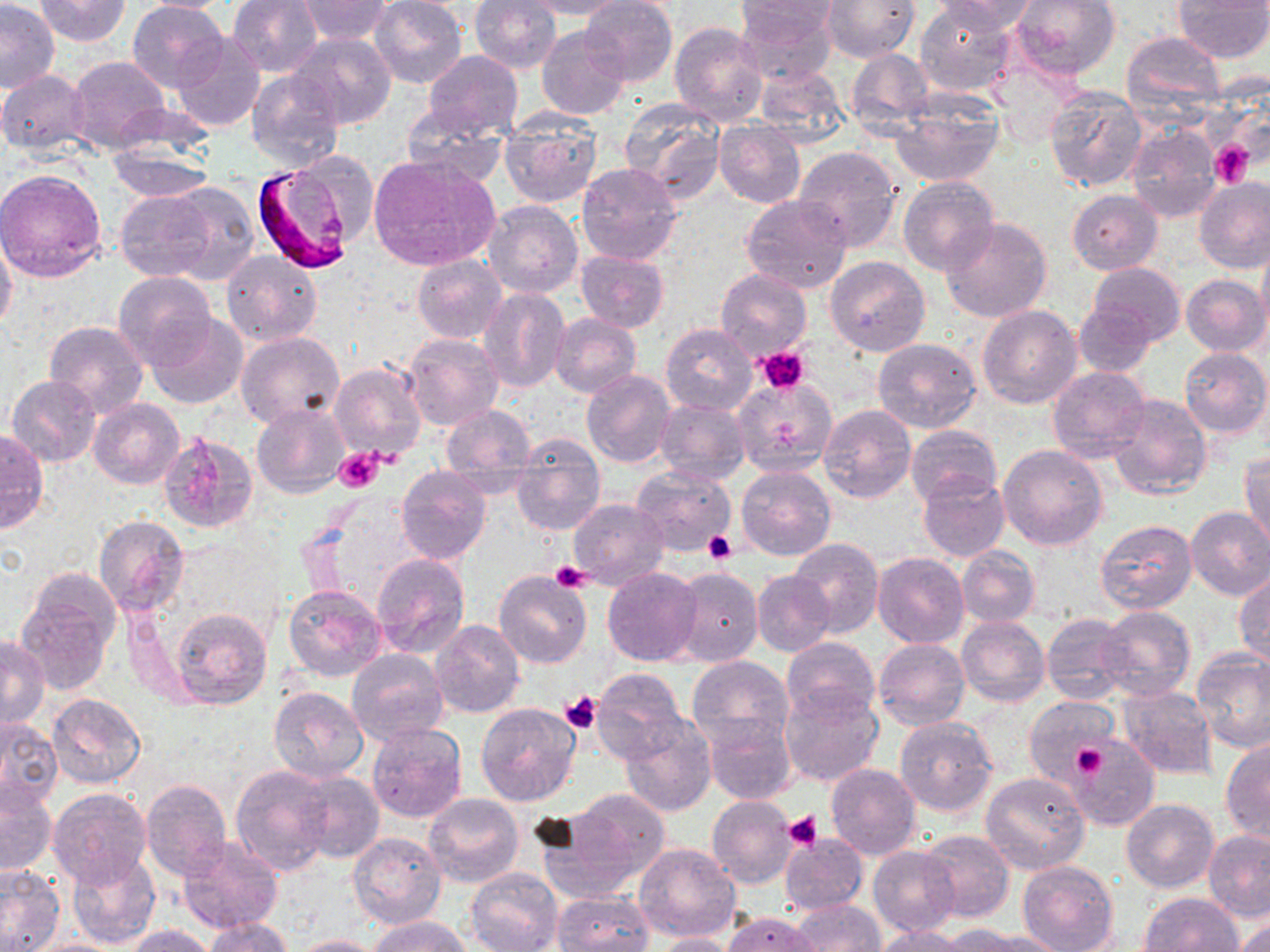

Approximate bounding boxes as named x1/y1/x2/y2 corners in pixels. Uninfected red blood cell locations: (x1=1, y1=0, x2=59, y2=92), (x1=35, y1=0, x2=131, y2=46), (x1=127, y1=0, x2=228, y2=92), (x1=129, y1=0, x2=242, y2=14), (x1=227, y1=0, x2=324, y2=75), (x1=296, y1=0, x2=392, y2=44), (x1=371, y1=0, x2=466, y2=89), (x1=470, y1=0, x2=561, y2=74), (x1=523, y1=0, x2=629, y2=18), (x1=931, y1=0, x2=1038, y2=35), (x1=1012, y1=0, x2=1121, y2=79), (x1=1174, y1=0, x2=1269, y2=62), (x1=580, y1=1, x2=678, y2=86), (x1=736, y1=1, x2=837, y2=87), (x1=821, y1=1, x2=919, y2=63), (x1=915, y1=2, x2=1015, y2=96), (x1=737, y1=3, x2=840, y2=37), (x1=670, y1=22, x2=768, y2=127), (x1=537, y1=25, x2=629, y2=120), (x1=286, y1=33, x2=399, y2=131), (x1=1121, y1=33, x2=1226, y2=120), (x1=173, y1=34, x2=266, y2=131), (x1=846, y1=49, x2=934, y2=134), (x1=423, y1=51, x2=523, y2=139), (x1=68, y1=55, x2=170, y2=151), (x1=752, y1=65, x2=850, y2=144), (x1=247, y1=69, x2=343, y2=171), (x1=0, y1=70, x2=91, y2=154), (x1=1045, y1=88, x2=1148, y2=192), (x1=891, y1=92, x2=1003, y2=187), (x1=619, y1=98, x2=726, y2=203), (x1=109, y1=100, x2=217, y2=164), (x1=401, y1=107, x2=509, y2=190), (x1=498, y1=113, x2=601, y2=207), (x1=712, y1=120, x2=805, y2=208), (x1=1124, y1=125, x2=1221, y2=223), (x1=106, y1=142, x2=214, y2=201), (x1=794, y1=146, x2=900, y2=250), (x1=369, y1=156, x2=500, y2=269), (x1=577, y1=162, x2=681, y2=265), (x1=0, y1=168, x2=107, y2=282), (x1=898, y1=177, x2=998, y2=277), (x1=1194, y1=179, x2=1270, y2=274), (x1=164, y1=184, x2=258, y2=282), (x1=116, y1=188, x2=218, y2=283), (x1=1067, y1=190, x2=1164, y2=275), (x1=741, y1=195, x2=853, y2=295), (x1=483, y1=200, x2=583, y2=298), (x1=939, y1=217, x2=1053, y2=323), (x1=0, y1=232, x2=17, y2=333), (x1=1257, y1=241, x2=1270, y2=336), (x1=576, y1=250, x2=670, y2=332), (x1=223, y1=251, x2=322, y2=347), (x1=412, y1=254, x2=506, y2=343), (x1=825, y1=256, x2=931, y2=356), (x1=1089, y1=263, x2=1185, y2=348), (x1=715, y1=268, x2=811, y2=361), (x1=114, y1=273, x2=216, y2=369), (x1=1181, y1=274, x2=1268, y2=356), (x1=478, y1=288, x2=570, y2=393), (x1=1075, y1=303, x2=1158, y2=377), (x1=978, y1=305, x2=1082, y2=409), (x1=147, y1=312, x2=249, y2=408), (x1=549, y1=314, x2=641, y2=396), (x1=44, y1=321, x2=149, y2=419), (x1=661, y1=324, x2=756, y2=415), (x1=236, y1=332, x2=346, y2=430), (x1=403, y1=333, x2=505, y2=432), (x1=874, y1=339, x2=982, y2=433), (x1=1180, y1=348, x2=1268, y2=439), (x1=328, y1=362, x2=426, y2=463), (x1=1048, y1=366, x2=1150, y2=463), (x1=581, y1=370, x2=675, y2=467), (x1=7, y1=375, x2=102, y2=466), (x1=552, y1=375, x2=646, y2=483), (x1=732, y1=378, x2=835, y2=473), (x1=1108, y1=394, x2=1211, y2=500), (x1=88, y1=398, x2=184, y2=489), (x1=657, y1=400, x2=751, y2=485), (x1=440, y1=402, x2=537, y2=488), (x1=253, y1=404, x2=350, y2=497), (x1=819, y1=404, x2=916, y2=502), (x1=907, y1=424, x2=1003, y2=508), (x1=0, y1=429, x2=48, y2=534), (x1=160, y1=432, x2=258, y2=532), (x1=511, y1=434, x2=606, y2=536), (x1=997, y1=444, x2=1108, y2=550), (x1=1241, y1=451, x2=1270, y2=553), (x1=631, y1=465, x2=737, y2=556), (x1=395, y1=466, x2=491, y2=564), (x1=738, y1=466, x2=835, y2=560), (x1=917, y1=473, x2=1009, y2=562), (x1=568, y1=498, x2=670, y2=589), (x1=1185, y1=506, x2=1270, y2=601), (x1=93, y1=515, x2=190, y2=618), (x1=1096, y1=519, x2=1197, y2=615), (x1=788, y1=539, x2=884, y2=638), (x1=958, y1=546, x2=1040, y2=627), (x1=873, y1=552, x2=968, y2=648), (x1=371, y1=555, x2=470, y2=659), (x1=603, y1=566, x2=702, y2=666), (x1=671, y1=566, x2=762, y2=667), (x1=753, y1=570, x2=835, y2=658), (x1=494, y1=572, x2=592, y2=670), (x1=1233, y1=572, x2=1270, y2=666), (x1=16, y1=577, x2=117, y2=694), (x1=282, y1=584, x2=387, y2=681), (x1=1098, y1=606, x2=1196, y2=701), (x1=169, y1=607, x2=273, y2=710), (x1=1042, y1=612, x2=1133, y2=704), (x1=958, y1=615, x2=1050, y2=707), (x1=429, y1=619, x2=525, y2=717), (x1=1, y1=635, x2=50, y2=727), (x1=782, y1=637, x2=879, y2=724), (x1=873, y1=637, x2=970, y2=730), (x1=346, y1=649, x2=450, y2=746), (x1=1192, y1=649, x2=1270, y2=752), (x1=687, y1=656, x2=792, y2=753), (x1=593, y1=668, x2=686, y2=763), (x1=779, y1=685, x2=885, y2=789), (x1=269, y1=686, x2=370, y2=783), (x1=1118, y1=686, x2=1218, y2=780), (x1=49, y1=694, x2=145, y2=789), (x1=1023, y1=696, x2=1118, y2=789), (x1=476, y1=702, x2=582, y2=806), (x1=704, y1=715, x2=797, y2=805), (x1=620, y1=716, x2=716, y2=817), (x1=0, y1=717, x2=62, y2=816), (x1=894, y1=717, x2=997, y2=816), (x1=367, y1=723, x2=466, y2=823), (x1=1069, y1=734, x2=1158, y2=830), (x1=1220, y1=739, x2=1270, y2=843), (x1=825, y1=762, x2=921, y2=859), (x1=229, y1=765, x2=336, y2=875), (x1=292, y1=769, x2=383, y2=863), (x1=980, y1=771, x2=1090, y2=874), (x1=140, y1=779, x2=232, y2=881), (x1=1, y1=780, x2=56, y2=876), (x1=47, y1=787, x2=152, y2=890), (x1=566, y1=787, x2=671, y2=884), (x1=423, y1=795, x2=523, y2=888), (x1=707, y1=796, x2=798, y2=889), (x1=1121, y1=799, x2=1219, y2=892), (x1=532, y1=812, x2=647, y2=904), (x1=919, y1=829, x2=1014, y2=923), (x1=1203, y1=830, x2=1270, y2=921), (x1=349, y1=833, x2=447, y2=930), (x1=780, y1=834, x2=867, y2=914), (x1=178, y1=839, x2=284, y2=932), (x1=634, y1=843, x2=740, y2=943), (x1=868, y1=847, x2=961, y2=937), (x1=66, y1=850, x2=161, y2=949), (x1=1017, y1=860, x2=1118, y2=952), (x1=0, y1=865, x2=65, y2=951), (x1=467, y1=867, x2=562, y2=952), (x1=553, y1=892, x2=655, y2=952), (x1=1139, y1=893, x2=1244, y2=952), (x1=791, y1=898, x2=883, y2=951), (x1=723, y1=912, x2=818, y2=951), (x1=368, y1=915, x2=473, y2=952), (x1=205, y1=916, x2=295, y2=952), (x1=1233, y1=920, x2=1270, y2=952), (x1=121, y1=924, x2=221, y2=952), (x1=872, y1=926, x2=973, y2=952), (x1=962, y1=928, x2=1066, y2=952), (x1=647, y1=932, x2=738, y2=952), (x1=291, y1=935, x2=389, y2=952), (x1=26, y1=937, x2=125, y2=952). Plasmodium falciparum-infected red blood cell locations: (x1=253, y1=160, x2=366, y2=274). Platelet locations: (x1=1209, y1=141, x2=1254, y2=186), (x1=756, y1=347, x2=811, y2=394), (x1=334, y1=448, x2=384, y2=493), (x1=703, y1=532, x2=735, y2=565), (x1=549, y1=561, x2=591, y2=593), (x1=560, y1=692, x2=602, y2=733), (x1=1072, y1=740, x2=1108, y2=780), (x1=784, y1=811, x2=823, y2=851). Slide-level diagnosis: Plasmodium falciparum. Optical microscopy. Image is 1270×952 pixels. Thin blood film. 1000x magnification. Single field of view. May-Grünwald-Giemsa stain.